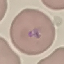
Result: malaria parasites detected. Thin smear of blood. Automatically extracted cell patch, resized to 64 × 64 pixels. Giemsa stain. Acquired by smartphone through the microscope eyepiece.